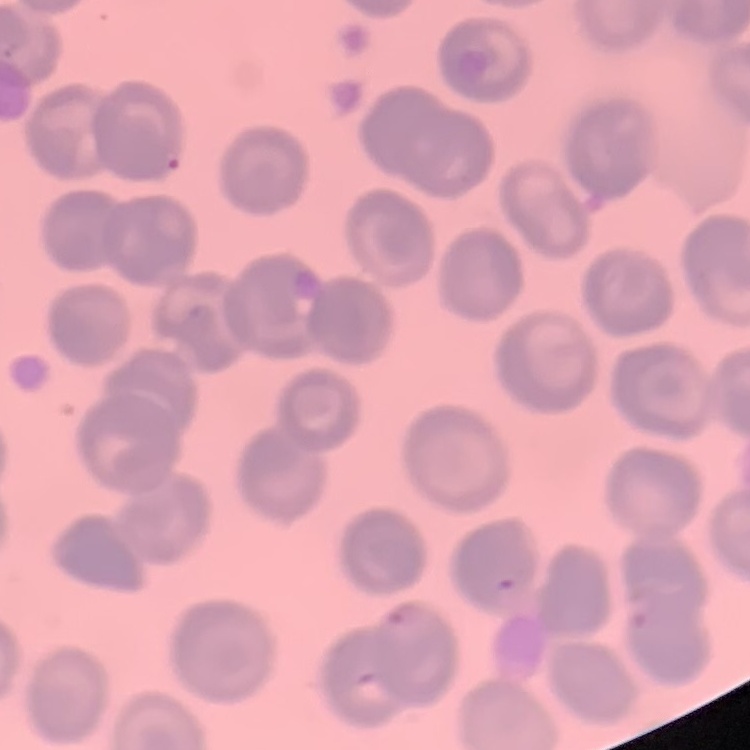
red blood cell morphology = no rouleaux formation
image type = one tile cut from a larger photomicrograph
preparation = thin peripheral smear
stain = Field's or Giemsa